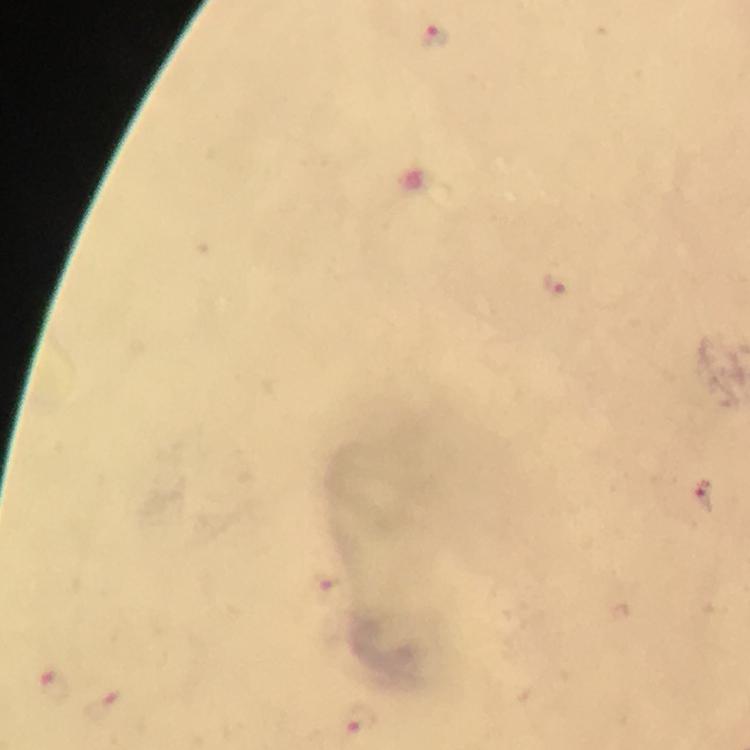
magnification = 100x
cropped from = one field of view
stain = Giemsa
capture = smartphone mounted on the microscope
malaria parasite locations = approximate centers as {x, y} in pixels: {437, 39}, {553, 286}, {705, 494}, {51, 687}, {102, 708}, {362, 718}
preparation = thick blood smear
immersion oil = used
context = from a diagnostic examination for malaria
image size = 750×750 pixels